Locate every Plasmodium falciparum-infected red blood cell.
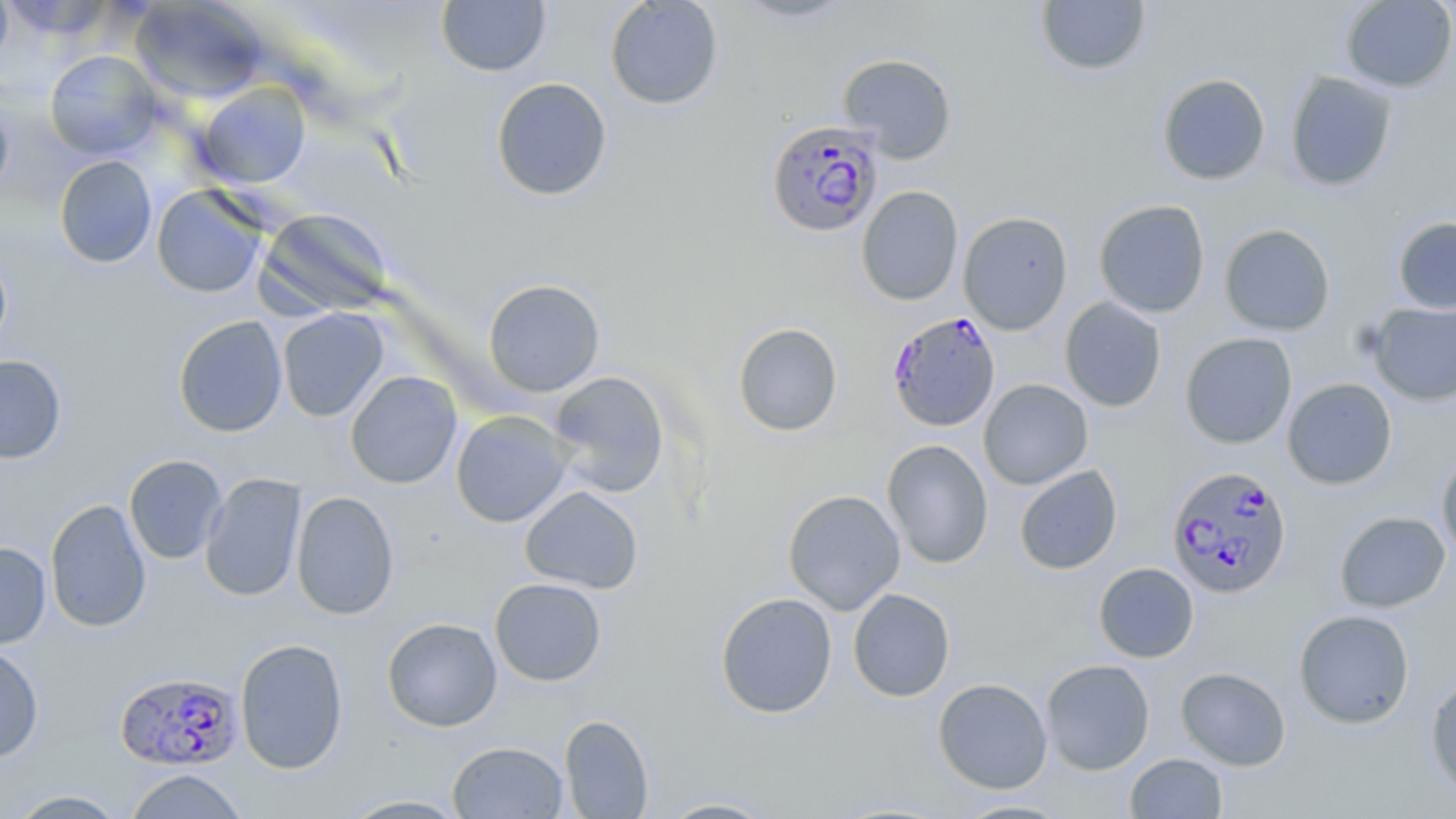

Approximate bounding boxes as (x1, y1, x2, y2) in pixels.
Plasmodium falciparum-infected red blood cells: (766, 120, 885, 238), (887, 312, 1001, 432), (1166, 465, 1293, 599), (115, 670, 243, 771).

slide-level diagnosis = Plasmodium falciparum
modality = optical microscopy
stain = May-Grünwald-Giemsa
preparation = thin blood film
image size = 1456×819 pixels
uninfected red blood cell locations = approximate bounding boxes as (x1, y1, x2, y2) in pixels: (0, 0, 13, 70), (436, 0, 551, 76), (605, 0, 724, 110), (733, 0, 854, 23), (1035, 0, 1151, 76), (1340, 0, 1456, 93), (129, 1, 267, 104), (44, 50, 162, 159), (837, 52, 957, 163), (1285, 70, 1397, 192), (1157, 73, 1271, 185), (490, 77, 613, 201), (195, 82, 312, 188), (0, 94, 15, 200), (54, 155, 158, 268), (151, 184, 268, 298), (856, 186, 964, 305), (1093, 199, 1210, 318), (258, 207, 393, 317), (958, 211, 1073, 334), (1393, 217, 1456, 314), (1219, 224, 1335, 335), (0, 249, 13, 358), (483, 279, 605, 397), (1060, 297, 1167, 412), (1368, 300, 1456, 406), (277, 308, 389, 421), (173, 315, 288, 437), (732, 322, 843, 437), (1180, 332, 1297, 449), (0, 355, 67, 464), (345, 370, 462, 489), (547, 371, 670, 498), (1282, 377, 1398, 490), (978, 379, 1093, 489), (450, 410, 574, 528), (881, 439, 994, 569), (1436, 451, 1456, 562), (124, 454, 228, 564), (1014, 465, 1123, 574), (200, 472, 307, 602), (520, 486, 644, 594), (782, 489, 906, 615), (290, 490, 400, 620), (45, 499, 152, 632), (1334, 510, 1451, 613), (0, 541, 51, 649), (1093, 562, 1199, 663), (489, 578, 607, 687), (848, 589, 956, 702), (715, 592, 838, 719), (1294, 609, 1415, 729), (381, 616, 503, 732), (234, 638, 349, 774), (0, 645, 44, 764), (1041, 659, 1155, 775), (1175, 667, 1291, 771), (1425, 675, 1456, 800), (933, 677, 1053, 794), (559, 714, 654, 819), (447, 741, 569, 818), (1125, 753, 1228, 818), (124, 769, 250, 818), (8, 790, 128, 818), (337, 794, 473, 818), (654, 796, 780, 818), (953, 798, 1072, 818)
magnification = 1000x
field of view = single